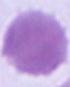
Summary:
  - Identification: red blood cell
  - Modality: micrograph
  - Magnification: 1000x